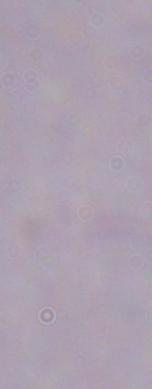

magnification = 1000x
modality = micrograph
identification = trypanosome